Give the extent of all Plasmodium vivax-infected red blood cells.
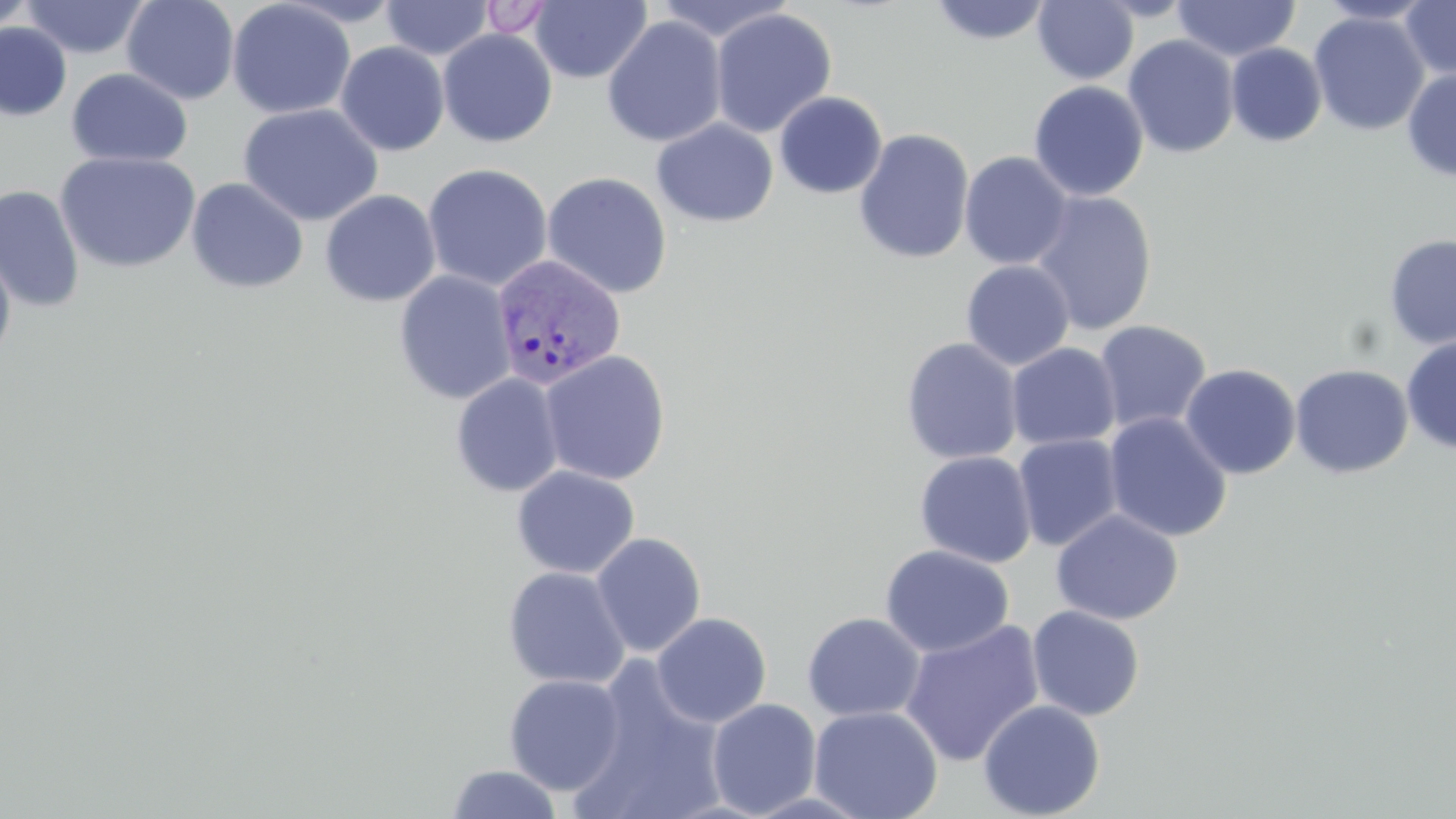

Approximate bounding boxes as (x1,y1)-(x2,y2) corner pairs in pixels.
Plasmodium vivax-infected red blood cells: (489,253)-(627,390).

Summary:
  - Uninfected red blood cell locations: (0,0)-(38,36), (20,0)-(150,59), (121,0)-(240,105), (227,0)-(356,120), (381,0)-(494,60), (652,0)-(798,43), (1400,0)-(1456,79), (476,1)-(559,39), (530,1)-(652,84), (927,1)-(1054,45), (1032,1)-(1139,85), (1172,1)-(1300,62), (1315,1)-(1436,25), (709,8)-(837,138), (1308,11)-(1430,136), (602,15)-(727,148), (0,23)-(72,120), (438,29)-(557,148), (1122,34)-(1240,159), (335,41)-(450,156), (1226,43)-(1327,147), (65,67)-(193,167), (1401,68)-(1456,181), (1028,80)-(1149,201), (774,91)-(887,199), (237,103)-(384,227), (651,119)-(778,227), (854,128)-(975,265), (55,151)-(201,274), (959,151)-(1073,270), (422,163)-(553,292), (541,171)-(673,299), (186,177)-(309,294), (0,184)-(85,313), (319,189)-(441,307), (1029,191)-(1158,335), (1384,234)-(1456,350), (0,246)-(17,370), (960,260)-(1075,370), (394,270)-(517,406), (1094,320)-(1212,434), (1401,334)-(1456,453), (900,338)-(1022,465), (1006,342)-(1121,451), (539,350)-(672,486), (1180,363)-(1301,480), (1290,363)-(1414,479), (450,373)-(565,497), (1103,412)-(1232,543), (1012,434)-(1124,552), (914,451)-(1037,568), (511,465)-(640,579), (1051,509)-(1183,626), (590,532)-(706,657), (880,544)-(1015,658), (502,566)-(630,690), (1027,605)-(1145,721), (651,612)-(772,728), (801,612)-(926,722), (899,620)-(1045,767), (566,669)-(731,819), (504,674)-(628,795), (706,698)-(822,817), (977,699)-(1105,818), (808,705)-(944,819), (445,764)-(565,819)
  - Slide-level diagnosis: Plasmodium vivax
  - Image size: 1456×819 pixels
  - Magnification: 1000x
  - Preparation: thin blood smear
  - Modality: optical microscopy
  - Field of view: single
  - Stain: May-Grünwald-Giemsa